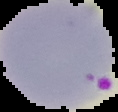
{
  "image_type": "segmented cell region on a black background",
  "preparation": "thin blood film",
  "image_size": "118×112 pixels",
  "malaria_status": "parasitized"
}